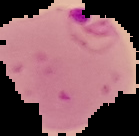
{
  "preparation": "thin blood film",
  "malaria_status": "parasitized",
  "image_size": "139×136 pixels",
  "image_type": "cell region segmented out of the field of view; surrounding area masked to black"
}